Assess this cell for malaria.
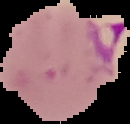
Parasitized.

Summary:
  - Image type: segmented cell region with the area outside set to black
  - Preparation: thin blood film
  - Image size: 130×124 pixels